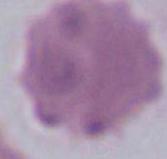 Micrograph. 1000x magnification. A red blood cell is shown.